Describe the morphology of the erythrocytes.
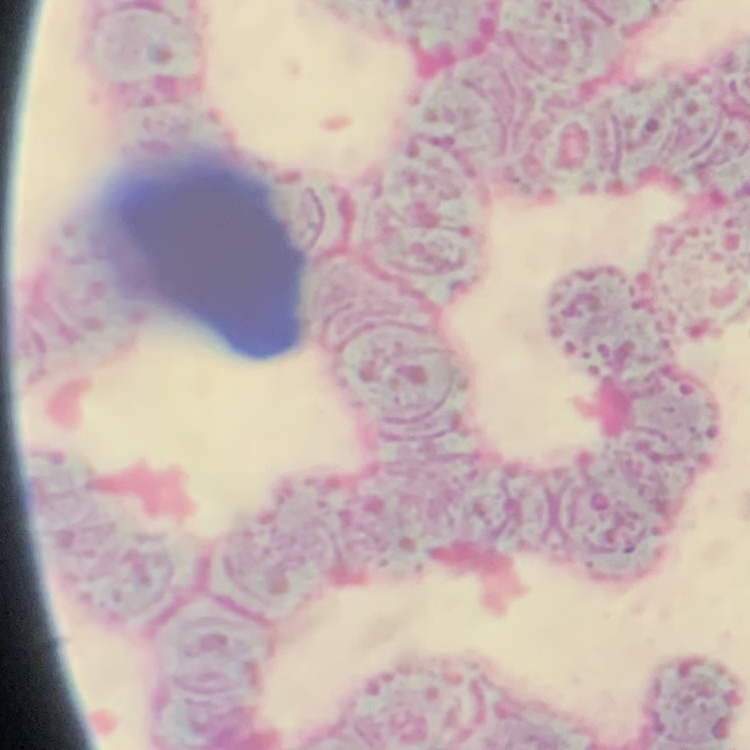

Rouleaux formation.

Summary:
  - Image type: one tile cut from a larger photomicrograph
  - Preparation: thin peripheral smear
  - Stain: Field's or Giemsa